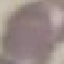

{
  "result": "no malaria parasites detected",
  "capture": "smartphone through the microscope eyepiece",
  "stain": "Giemsa",
  "preparation": "thin blood film",
  "image_type": "cell patch, automatically extracted from a larger field of view and resized to 64 × 64 pixels"
}